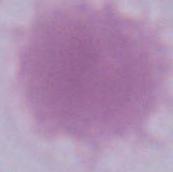
modality = micrograph
identification = erythrocyte
magnification = 1000x